Locate every Plasmodium parasite.
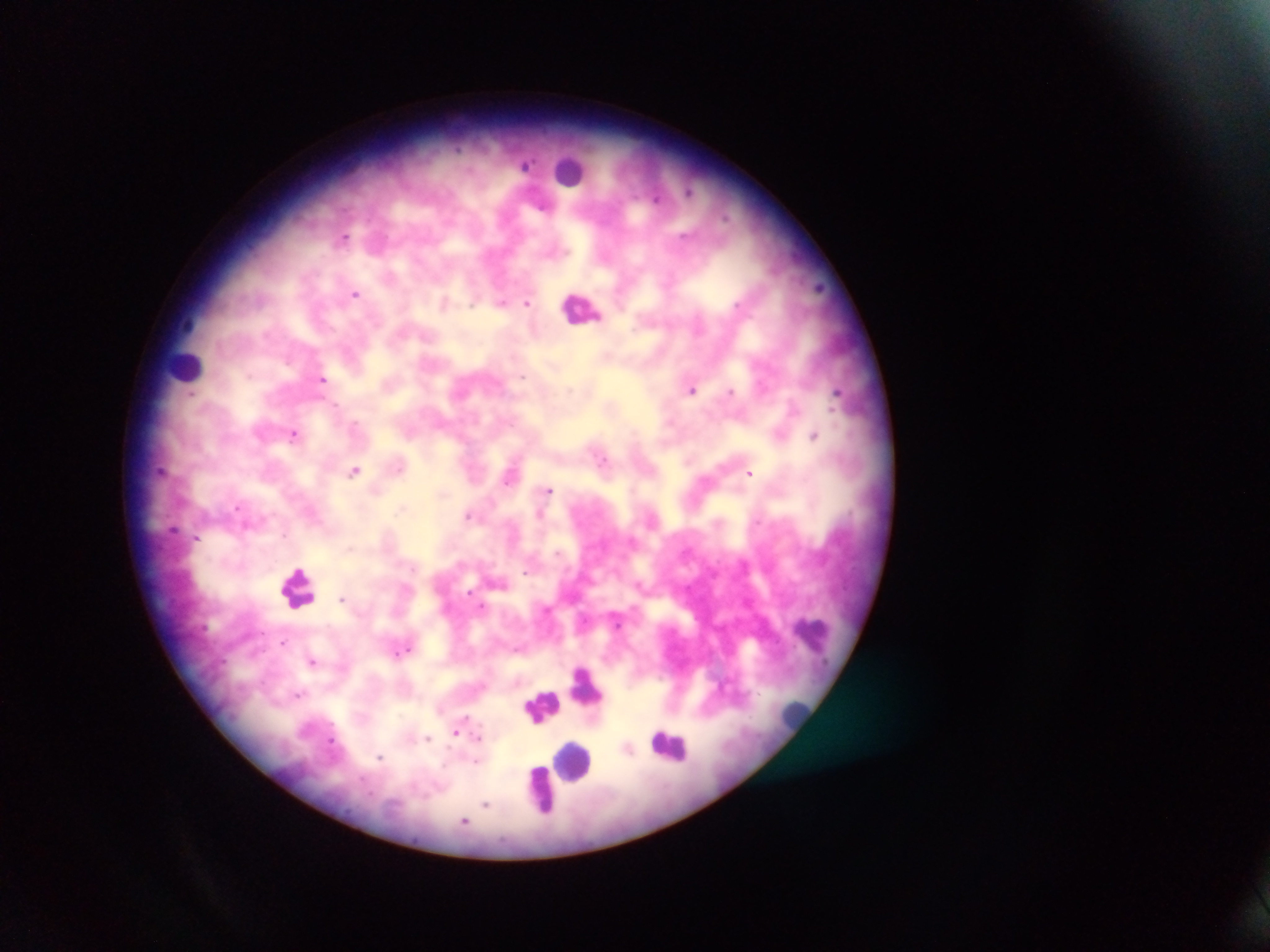
Approximate centers as x y in pixels.
Plasmodium parasites: 526 164; 690 191; 727 217; 344 238; 356 293; 502 302; 527 302; 247 376; 523 376; 323 378; 692 388; 571 391; 731 391; 837 392; 191 394; 336 405; 833 409; 354 424; 293 434; 814 435; 603 459; 354 471; 750 473; 508 481; 549 490; 237 507; 400 509; 539 514; 468 515; 284 535; 197 538; 349 548; 558 552; 412 567; 526 572; 469 591; 341 598; 482 605; 547 610; 618 625; 263 633; 285 643; 404 650; 313 661; 299 695; 464 716; 456 734; 478 737; 427 738; 331 742; 380 758; 475 761; 486 805; 465 821.

{
  "leukocyte_locations": "approximate centers as x y in pixels: 572 170; 582 307; 188 365; 298 587; 812 635; 587 688; 561 695; 542 706; 794 712; 671 745; 574 760; 541 790",
  "preparation": "thick blood film",
  "capture": "mobile-phone photograph through a microscope",
  "image_size": "1270×952 pixels",
  "country": "Ghana",
  "field_of_view": "single"
}